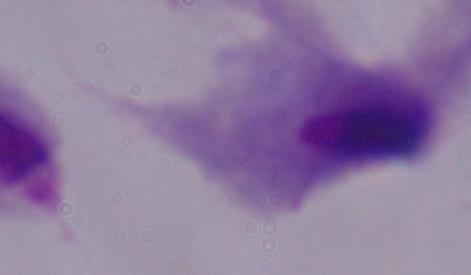
magnification: 1000x
modality: micrograph
identification: trichomonad